State which cell type is depicted.
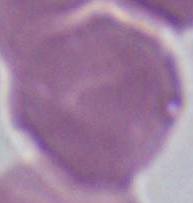

This is an erythrocyte.

Summary:
  - Magnification: 1000x
  - Modality: photomicrograph